Give the position of every malaria parasite.
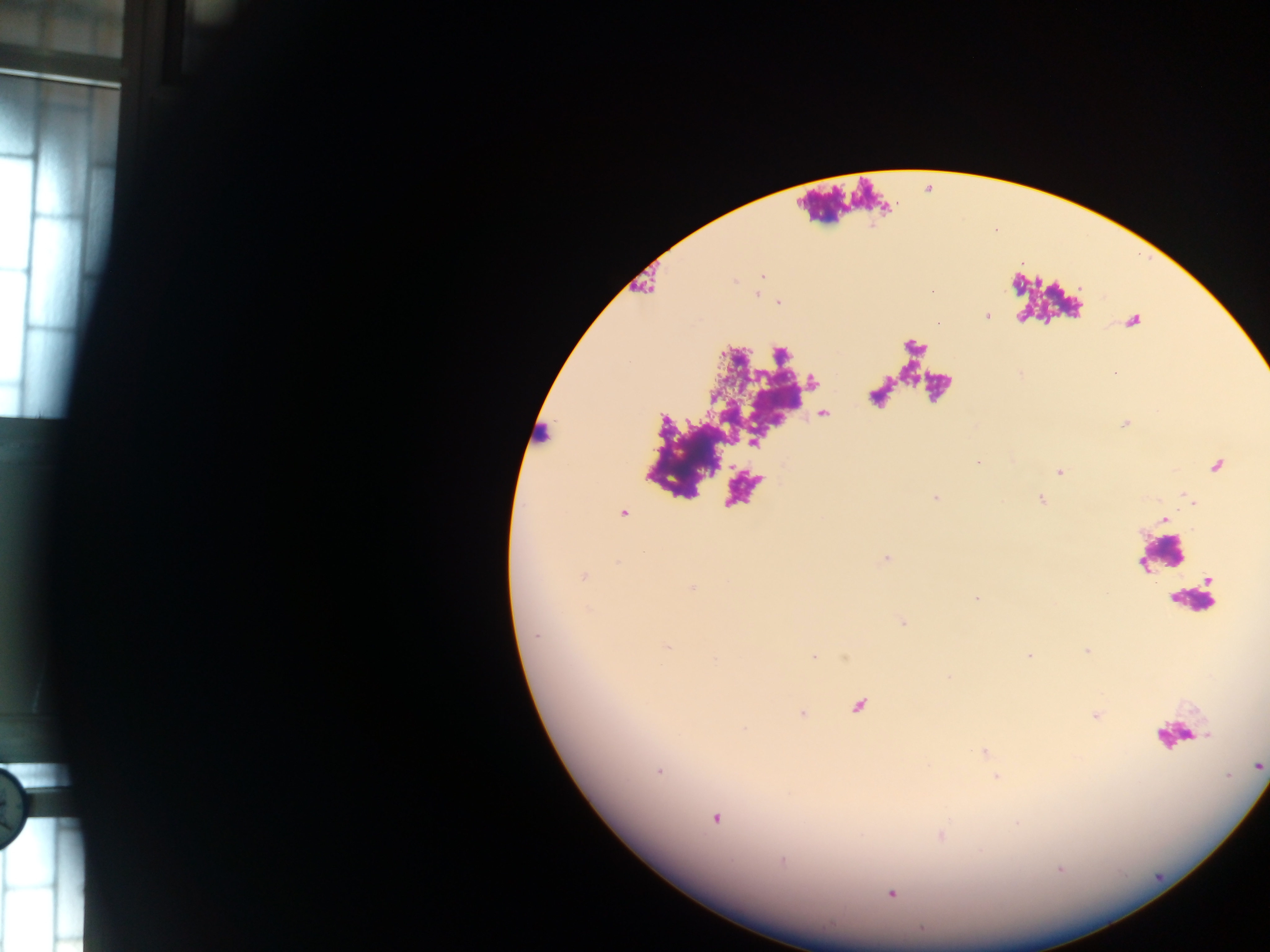

Approximate centers as x y in pixels.
Malaria parasites: 762 275; 757 294; 986 314; 979 462; 1058 471; 935 498; 1041 499; 622 513; 885 559; 582 576; 976 597; 902 621; 666 645; 1028 655; 814 656; 857 706; 802 713; 1096 716; 984 753; 1258 765; 659 771; 997 776; 715 817; 940 836; 890 894.

field of view = single
capture = mobile-phone photograph through a microscope
country = Ghana
preparation = thick blood smear
leukocyte locations = approximate centers as x y in pixels: 536 436; 1193 600
image size = 1270×952 pixels